Which red blood cells are Plasmodium falciparum-infected, and which are of indeterminate infection status?
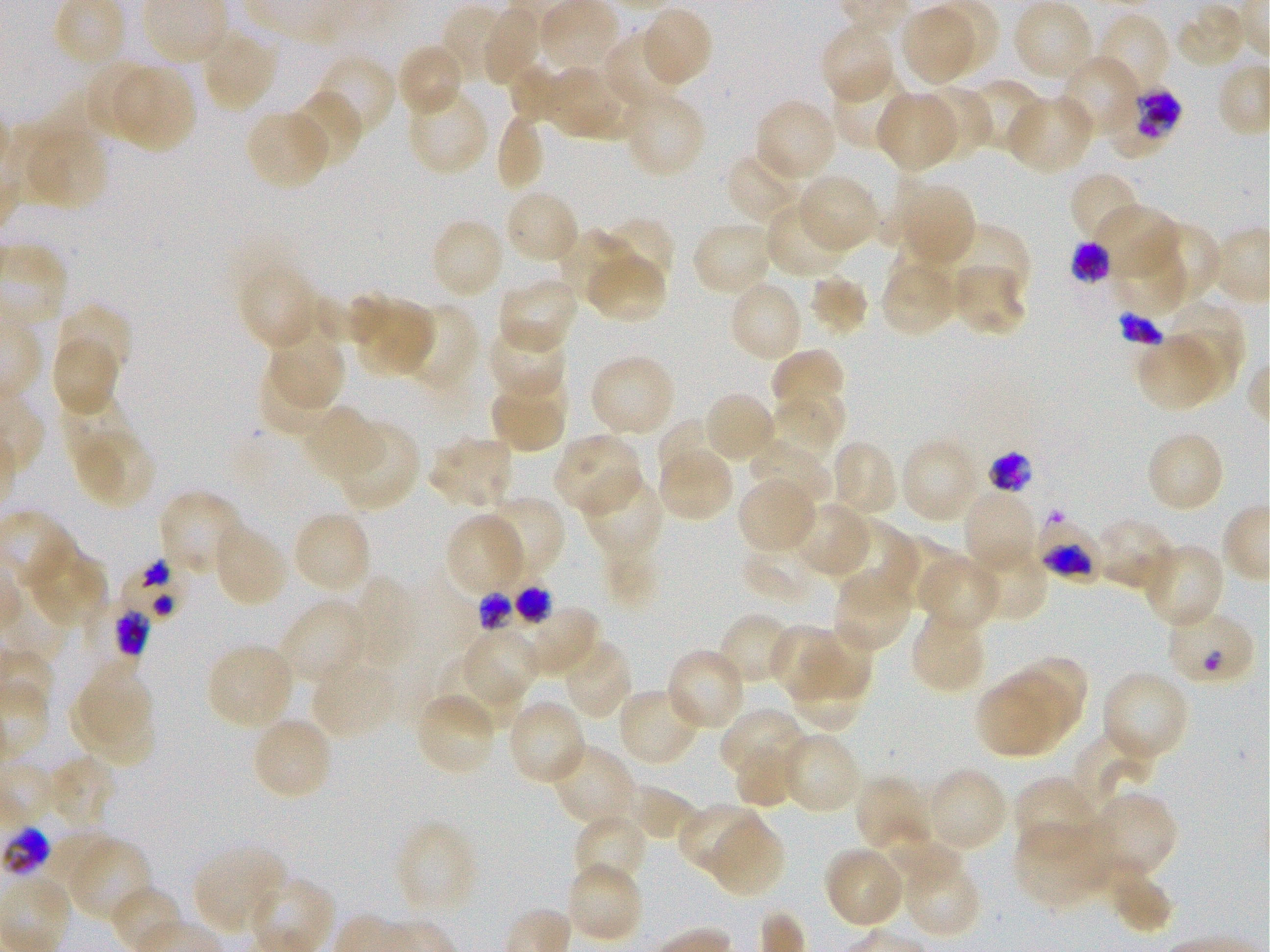
Approximate bounding boxes as {x1, y1, x2, y2} in pixels. Not every red blood cell is marked. A life-cycle stage — or a range of stages, where the recorded stages span more than one — follows each staged infected red blood cell.
Infected red blood cells: {1104, 88, 1183, 155} early trophozoite to early schizont; {1074, 245, 1110, 286}; {984, 452, 1039, 490} late trophozoite to early schizont; {1036, 509, 1101, 579} late trophozoite to early schizont; {120, 554, 191, 624}; {513, 584, 562, 632}; {1164, 607, 1256, 686} early ring; {112, 613, 156, 657}.
Red blood cells of indeterminate infection status: {474, 586, 520, 636}.

Locations of uninfected red blood cells: {1013, 0, 1095, 84}, {440, 3, 516, 86}, {481, 5, 545, 87}, {898, 5, 979, 87}, {1174, 5, 1249, 71}, {637, 7, 713, 90}, {1096, 11, 1172, 96}, {820, 21, 896, 105}, {200, 29, 277, 113}, {605, 29, 686, 112}, {397, 43, 466, 119}, {1059, 53, 1142, 143}, {313, 54, 396, 139}, {85, 60, 158, 143}, {111, 63, 195, 154}, {573, 63, 641, 141}, {542, 64, 619, 136}, {510, 65, 565, 123}, {831, 69, 911, 150}, {963, 78, 1046, 154}, {406, 85, 490, 177}, {917, 86, 992, 163}, {622, 89, 706, 180}, {286, 90, 363, 174}, {875, 91, 961, 173}, {1005, 93, 1095, 176}, {754, 98, 838, 183}, {245, 109, 332, 191}, {495, 112, 544, 194}, {22, 124, 109, 212}, {727, 147, 813, 224}, {1069, 170, 1143, 245}, {795, 173, 880, 254}, {907, 182, 976, 258}, {503, 188, 581, 265}, {765, 202, 850, 280}, {1093, 203, 1181, 283}, {595, 217, 674, 298}, {429, 218, 506, 300}, {691, 220, 775, 297}, {935, 221, 1031, 298}, {1145, 221, 1221, 297}, {558, 228, 637, 309}, {893, 233, 963, 287}, {1113, 248, 1183, 314}, {586, 250, 666, 324}, {240, 262, 322, 352}, {881, 267, 955, 333}, {807, 275, 869, 336}, {497, 277, 578, 356}, {727, 280, 804, 364}, {315, 293, 388, 344}, {359, 297, 434, 375}, {1160, 300, 1245, 393}, {407, 302, 479, 393}, {56, 304, 133, 385}, {487, 321, 567, 401}, {50, 333, 120, 415}, {1136, 333, 1227, 411}, {274, 336, 346, 406}, {770, 348, 846, 423}, {589, 353, 677, 438}, {258, 365, 337, 439}, {488, 377, 568, 453}, {768, 390, 844, 460}, {703, 391, 777, 464}, {62, 403, 137, 470}, {300, 406, 383, 485}, {1034, 411, 1111, 489}, {658, 419, 722, 488}, {334, 420, 420, 512}, {73, 425, 155, 508}, {1146, 430, 1226, 513}, {551, 432, 643, 518}, {428, 433, 517, 511}, {898, 437, 982, 525}, {829, 439, 899, 520}, {749, 440, 833, 509}, {656, 442, 734, 524}, {580, 473, 665, 563}, {736, 476, 818, 555}, {962, 488, 1040, 575}, {160, 490, 247, 581}, {479, 496, 565, 584}, {789, 501, 873, 579}, {291, 510, 372, 597}, {444, 512, 527, 597}, {1093, 517, 1178, 593}, {833, 521, 917, 608}, {212, 523, 288, 608}, {882, 533, 964, 613}, {1139, 543, 1224, 630}, {22, 545, 109, 629}, {967, 546, 1048, 623}, {739, 549, 820, 605}, {918, 555, 1000, 634}, {832, 569, 915, 654}, {348, 576, 419, 683}, {278, 599, 368, 686}, {493, 602, 598, 677}, {909, 610, 988, 694}, {717, 611, 795, 685}, {769, 625, 835, 701}, {810, 629, 876, 694}, {463, 630, 537, 705}, {559, 638, 634, 720}, {206, 642, 296, 731}, {665, 648, 747, 732}, {436, 654, 524, 734}, {792, 655, 863, 730}, {311, 656, 398, 740}, {1029, 657, 1086, 712}, {81, 665, 155, 745}, {1099, 668, 1189, 764}, {998, 675, 1072, 749}, {979, 683, 1046, 756}, {616, 688, 702, 768}, {67, 692, 155, 762}, {414, 692, 498, 777}, {505, 698, 588, 786}, {719, 708, 807, 785}, {251, 715, 334, 801}, {1071, 730, 1154, 817}, {780, 732, 861, 815}, {734, 742, 799, 809}, {549, 743, 637, 830}, {44, 755, 117, 833}, {922, 765, 1009, 854}, {854, 774, 934, 854}, {1015, 776, 1099, 858}, {617, 785, 697, 841}, {1087, 793, 1177, 881}, {677, 802, 766, 878}, {572, 813, 648, 888}, {708, 816, 784, 898}, {1015, 818, 1117, 909}, {394, 821, 479, 916}, {67, 838, 153, 926}, {874, 838, 962, 887}, {192, 844, 288, 936}, {824, 846, 906, 929}, {900, 854, 981, 938}, {565, 860, 644, 945}, {1106, 865, 1174, 932}, {110, 885, 187, 944}. Plasmodium falciparum strain 3D7 in static in-vitro culture. Image is 1270×952 pixels. 100x objective under oil immersion, numerical aperture 1.25. Donor blood group O+. Thin blood film. Giemsa-stained preparation. One field from this slide.